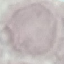
malaria status = uninfected
capture = smartphone camera at the microscope eyepiece
preparation = thin blood smear
image type = automatically extracted cell patch, resized to 64 × 64 pixels
stain = Giemsa